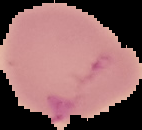

Summary:
  - Result: negative for malaria parasites
  - Preparation: thin blood smear
  - Image size: 142×130 pixels
  - Image type: segmented cell region with the area outside set to black